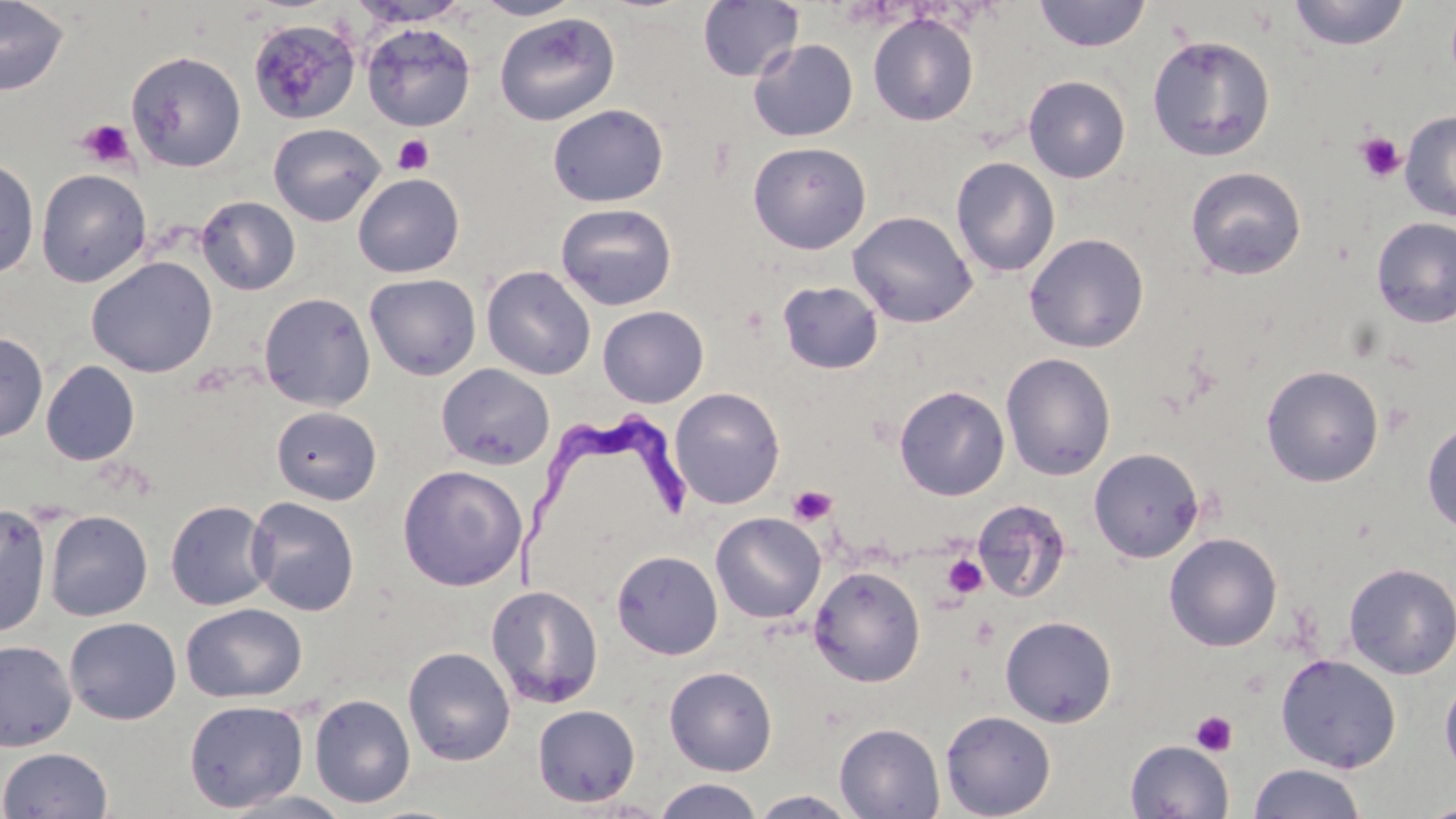
Summary:
  - Coordinate format: approximate bounding boxes as (x1, y1, x2, y2) in pixels
  - Platelet locations: (77, 118, 136, 169), (1355, 132, 1406, 183), (393, 134, 435, 175), (788, 484, 837, 525), (942, 554, 988, 599), (1191, 711, 1237, 756)
  - Uninfected red blood cell locations: (0, 0, 70, 95), (476, 0, 582, 20), (1033, 0, 1151, 52), (1289, 0, 1410, 50), (350, 1, 468, 27), (697, 1, 804, 82), (494, 12, 621, 126), (867, 13, 979, 126), (248, 18, 360, 125), (360, 23, 476, 131), (1147, 34, 1276, 162), (748, 39, 859, 142), (127, 50, 246, 172), (1023, 75, 1131, 183), (547, 103, 669, 207), (1399, 110, 1456, 222), (268, 122, 385, 226), (748, 141, 872, 254), (0, 155, 40, 280), (951, 157, 1060, 278), (1185, 166, 1307, 280), (36, 168, 152, 287), (353, 173, 465, 278), (196, 196, 300, 295), (555, 203, 677, 310), (847, 210, 977, 328), (1371, 217, 1456, 328), (1024, 233, 1149, 352), (87, 256, 217, 377), (481, 265, 596, 380), (365, 273, 481, 380), (778, 281, 883, 374), (259, 292, 376, 410), (598, 306, 709, 407), (0, 331, 48, 442), (1001, 353, 1116, 481), (41, 361, 140, 465), (436, 363, 555, 470), (1261, 365, 1384, 487), (894, 385, 1010, 501), (669, 387, 785, 509), (271, 406, 381, 505), (1422, 419, 1456, 535), (1088, 447, 1204, 562), (397, 465, 527, 591), (246, 497, 360, 616), (972, 498, 1071, 603), (165, 500, 274, 611), (0, 504, 52, 639), (45, 510, 153, 621), (710, 512, 826, 623), (1164, 533, 1283, 652), (612, 550, 723, 660), (1343, 562, 1456, 679), (808, 565, 926, 687), (486, 584, 604, 709), (181, 603, 307, 703), (1000, 615, 1117, 727), (64, 617, 181, 725), (0, 640, 76, 751), (403, 646, 515, 766), (1276, 653, 1401, 773), (664, 666, 777, 776), (1440, 676, 1456, 777), (309, 694, 416, 808), (183, 699, 308, 812), (532, 704, 640, 806), (940, 710, 1056, 819), (834, 722, 945, 818), (1126, 740, 1234, 819), (0, 747, 113, 818), (1248, 763, 1366, 819), (654, 778, 763, 819), (219, 790, 355, 818), (749, 790, 859, 818), (1417, 802, 1456, 819)
  - Trypanosoma brucei locations: (515, 411, 688, 592)
  - Slide-level diagnosis: Trypanosoma brucei
  - Stain: May-Grünwald-Giemsa
  - Modality: optical microscopy
  - Magnification: 1000x
  - Preparation: thin blood smear
  - Field of view: one of a larger specimen
  - Image size: 1456×819 pixels